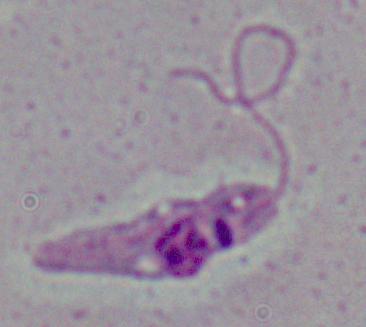 A Leishmania parasite is shown. 1000x magnification. Micrograph.